Mark where platelets are.
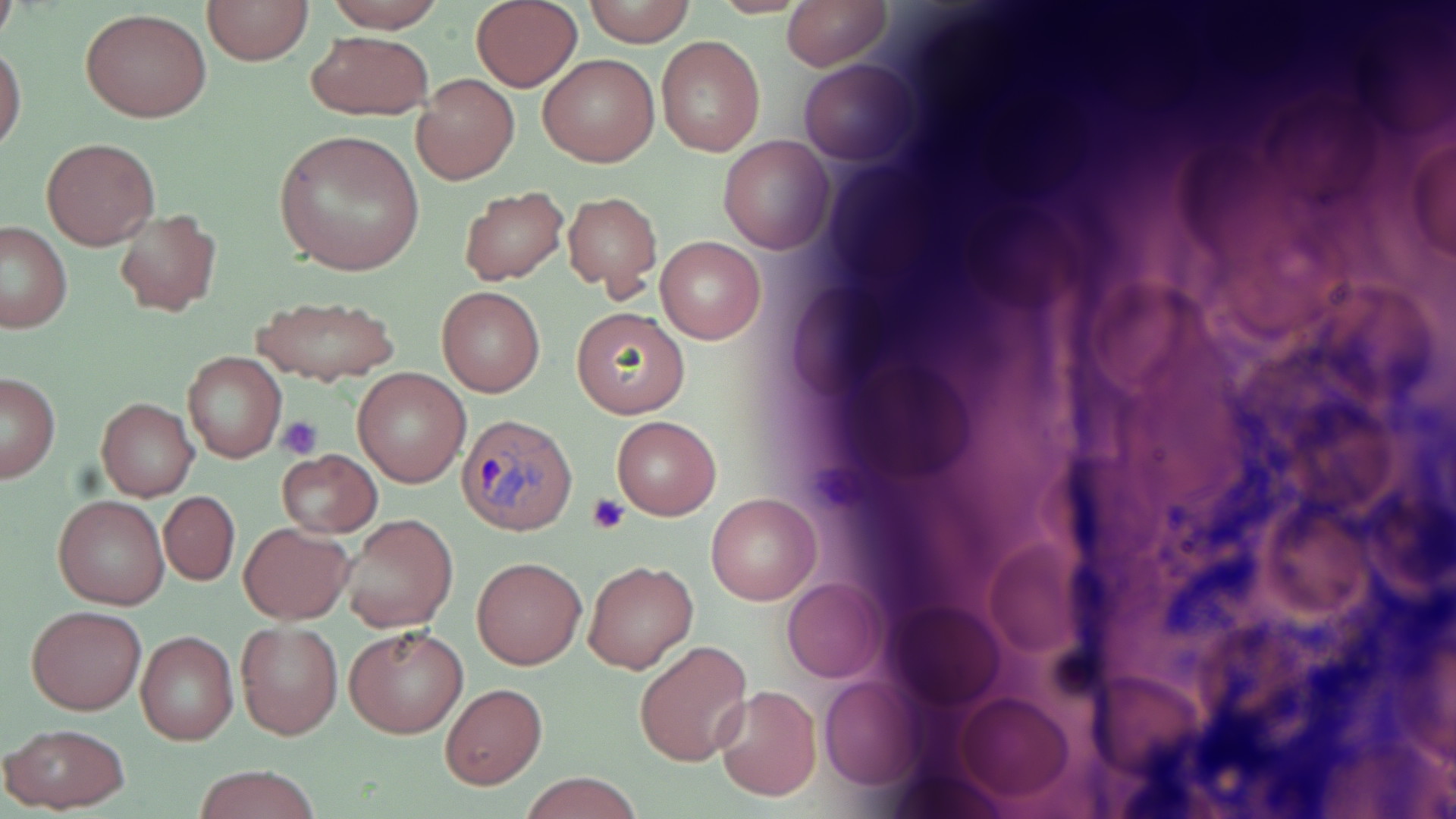

Approximate bounding boxes as named x1/y1/x2/y2 corners in pixels.
Platelets: (x1=278, y1=416, x2=324, y2=459), (x1=586, y1=493, x2=629, y2=535).

slide-level diagnosis = Plasmodium ovale
preparation = thin blood film
Plasmodium ovale-infected red blood cell locations = approximate bounding boxes as named x1/y1/x2/y2 corners in pixels: (x1=459, y1=412, x2=577, y2=534)
image size = 1456×819 pixels
field of view = one of a larger specimen
uninfected red blood cell locations = approximate bounding boxes as named x1/y1/x2/y2 corners in pixels: (x1=203, y1=0, x2=313, y2=65), (x1=323, y1=0, x2=447, y2=32), (x1=582, y1=0, x2=696, y2=47), (x1=780, y1=0, x2=891, y2=71), (x1=471, y1=2, x2=582, y2=90), (x1=0, y1=3, x2=18, y2=53), (x1=80, y1=7, x2=212, y2=123), (x1=304, y1=31, x2=432, y2=120), (x1=656, y1=35, x2=765, y2=157), (x1=1, y1=42, x2=26, y2=156), (x1=538, y1=55, x2=658, y2=167), (x1=799, y1=60, x2=918, y2=166), (x1=412, y1=74, x2=519, y2=185), (x1=1408, y1=122, x2=1456, y2=271), (x1=273, y1=129, x2=425, y2=276), (x1=719, y1=135, x2=835, y2=254), (x1=43, y1=137, x2=160, y2=250), (x1=457, y1=185, x2=569, y2=286), (x1=563, y1=191, x2=662, y2=297), (x1=114, y1=208, x2=222, y2=316), (x1=0, y1=222, x2=73, y2=333), (x1=656, y1=235, x2=766, y2=344), (x1=437, y1=286, x2=545, y2=397), (x1=254, y1=295, x2=398, y2=387), (x1=569, y1=306, x2=691, y2=419), (x1=181, y1=352, x2=287, y2=462), (x1=352, y1=366, x2=469, y2=486), (x1=0, y1=372, x2=61, y2=482), (x1=96, y1=397, x2=198, y2=502), (x1=610, y1=416, x2=721, y2=519), (x1=277, y1=449, x2=381, y2=538), (x1=158, y1=491, x2=239, y2=586), (x1=54, y1=494, x2=168, y2=610), (x1=705, y1=494, x2=820, y2=605), (x1=340, y1=514, x2=457, y2=634), (x1=240, y1=523, x2=353, y2=624), (x1=980, y1=537, x2=1091, y2=669), (x1=472, y1=556, x2=585, y2=669), (x1=584, y1=560, x2=698, y2=674), (x1=782, y1=579, x2=884, y2=683), (x1=889, y1=601, x2=1004, y2=712), (x1=26, y1=605, x2=145, y2=715), (x1=236, y1=621, x2=343, y2=741), (x1=345, y1=625, x2=467, y2=737), (x1=135, y1=630, x2=238, y2=744), (x1=634, y1=641, x2=752, y2=766), (x1=818, y1=672, x2=926, y2=790), (x1=1089, y1=672, x2=1205, y2=776), (x1=440, y1=683, x2=547, y2=788), (x1=714, y1=684, x2=821, y2=801), (x1=953, y1=693, x2=1071, y2=804), (x1=1, y1=723, x2=131, y2=812), (x1=193, y1=765, x2=321, y2=819), (x1=516, y1=773, x2=648, y2=819)
magnification = 1000x
stain = May-Grünwald-Giemsa
modality = optical microscopy